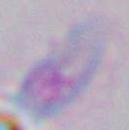
Micrograph. 1000x magnification. Toxoplasma gondii is seen.